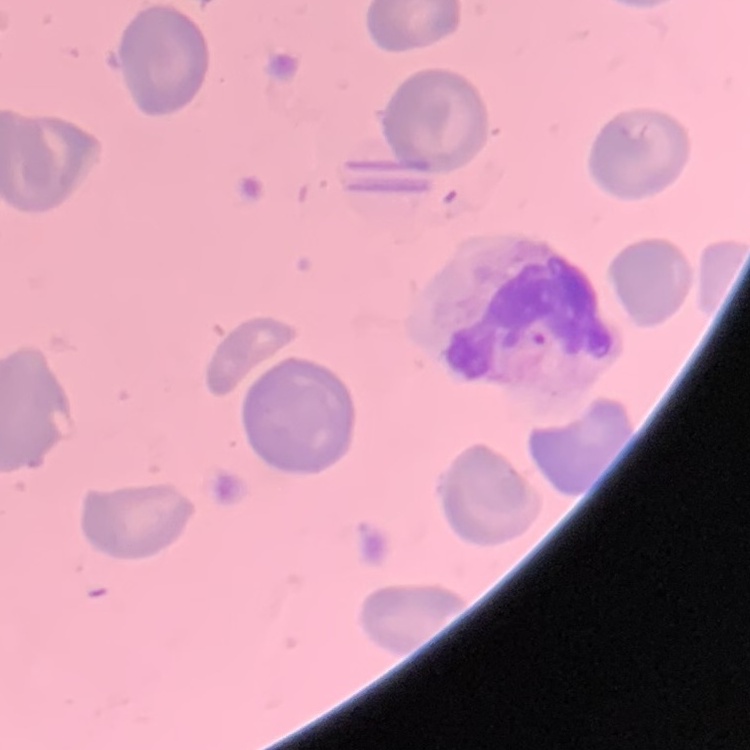

Summary:
  - Erythrocyte morphology: no rouleaux formation
  - Image type: square crop of a larger photomicrograph
  - Preparation: thin blood film
  - Stain: Field's or Giemsa